Comment on the morphology of the erythrocytes.
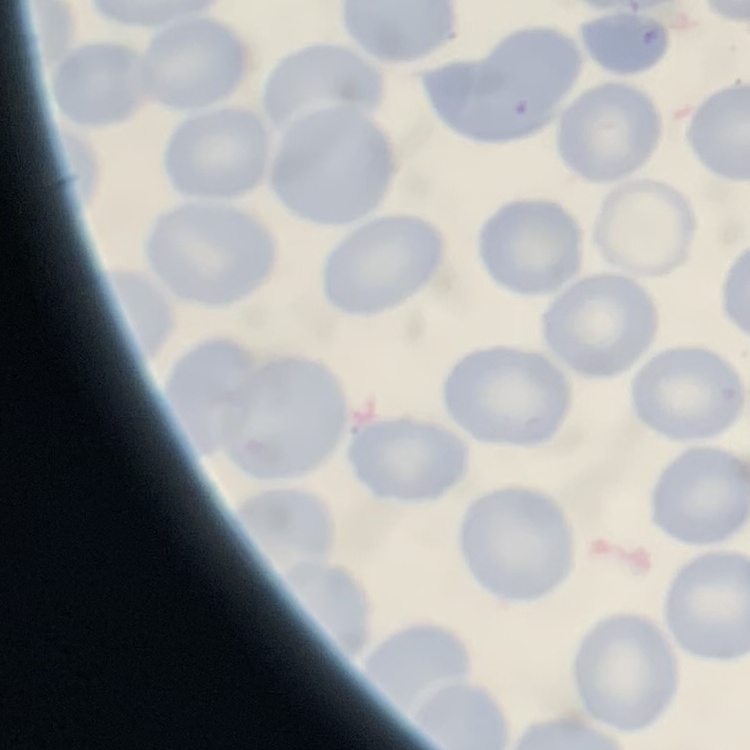
They show no rouleaux formation.

Square crop of a larger photomicrograph. Thin peripheral smear. Field's or Giemsa stain.